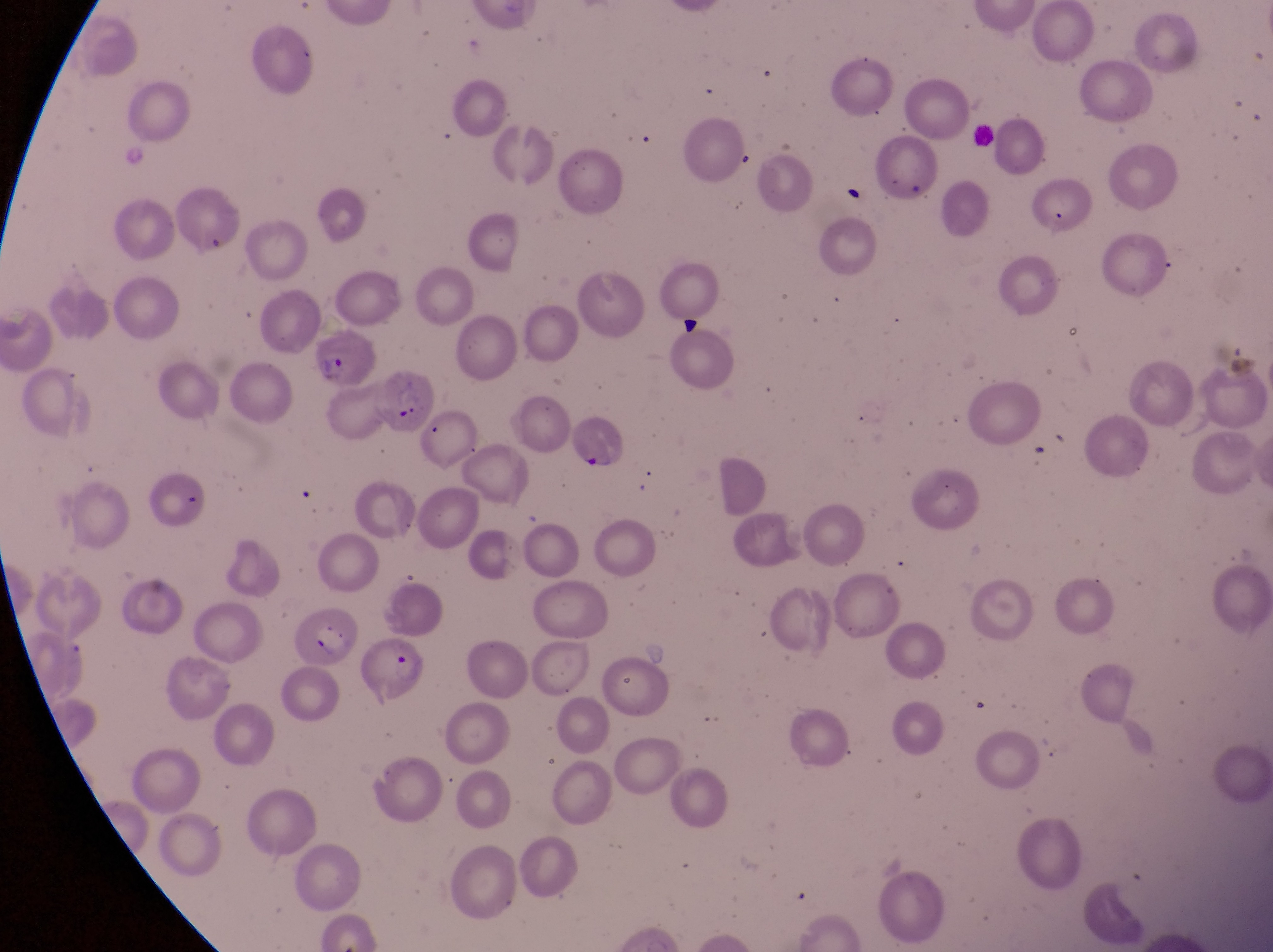
field of view = single
image size = 1273×952 pixels
magnification = 1000x
capture = smartphone photograph through the eyepiece of an Olympus CX-23 microscope
parasitised red blood cell locations = approximate bounding boxes as (left, top, right, bottom) in pixels: (174, 189, 241, 259), (307, 332, 379, 387), (373, 370, 435, 431), (565, 410, 622, 477), (277, 607, 360, 667), (359, 635, 429, 700)
country = Uganda
preparation = thin blood smear